Describe the morphology of the erythrocytes.
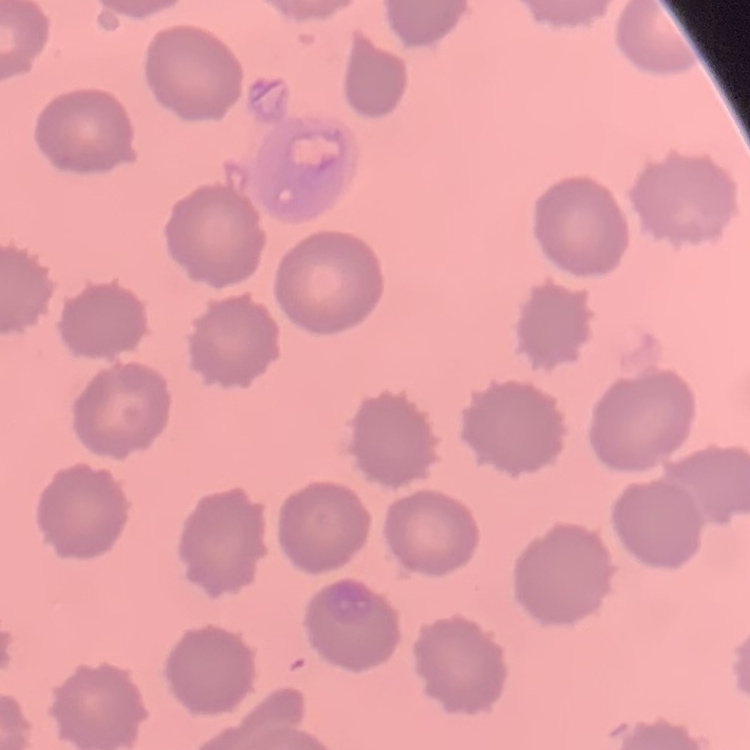
No rouleaux formation.

preparation = thin peripheral smear
stain = Field's or Giemsa
image type = square crop of a larger photomicrograph